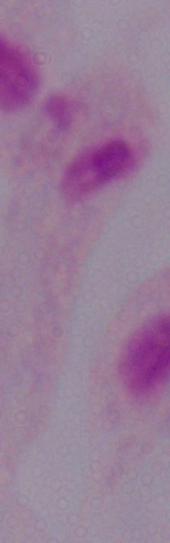
Summary:
  - Modality: micrograph
  - Identification: trichomonad
  - Magnification: 1000x